Classify this cell by malaria status.
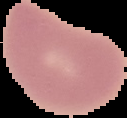
It is uninfected.

Summary:
  - Image size: 127×118 pixels
  - Preparation: thin blood film
  - Image type: segmented cell region on a black background